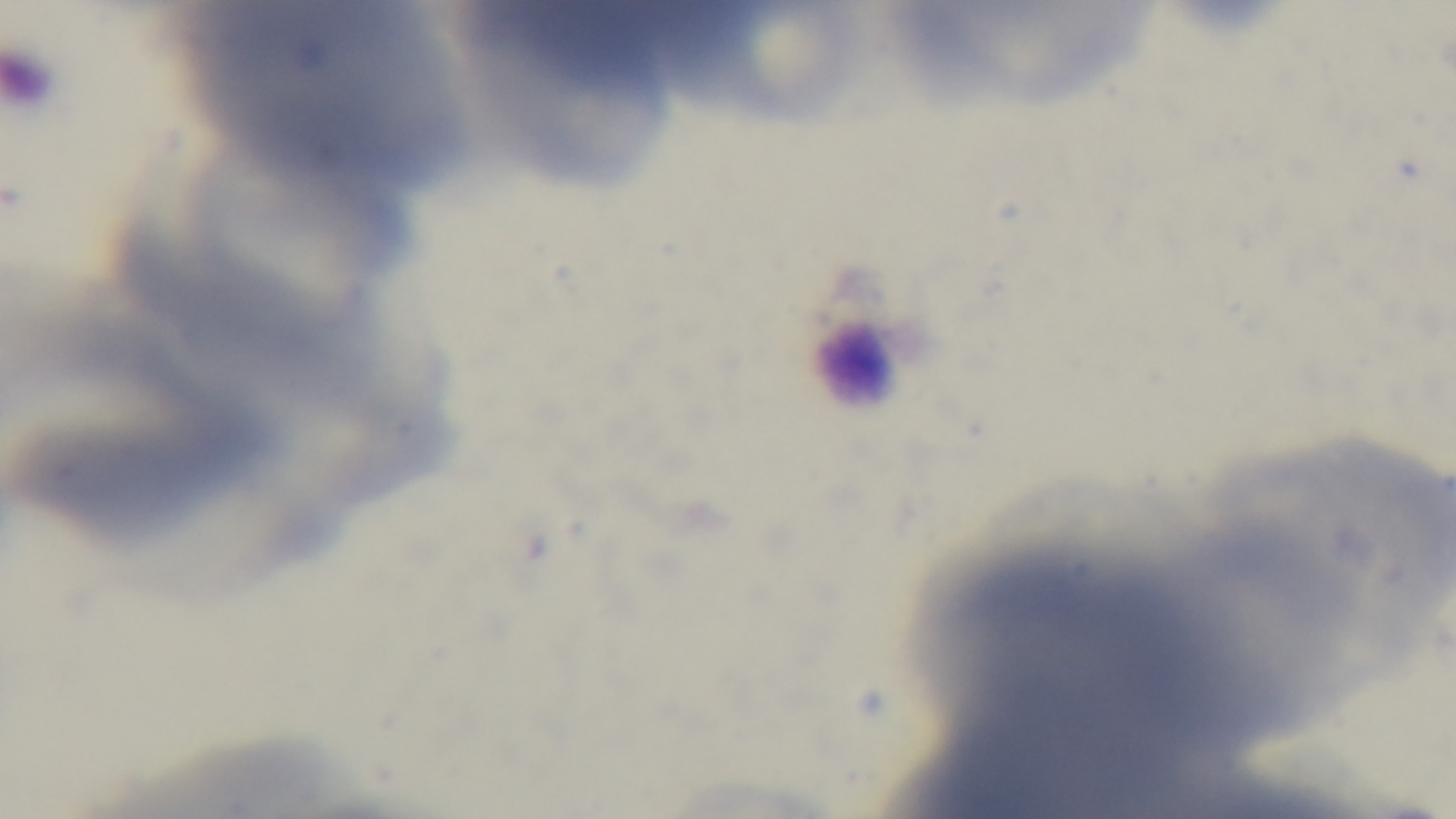

stain = Giemsa
capture = mounted 4K digital camera
preparation = thin blood film
malaria status = uninfected
modality = light microscopy
objective = 100x oil immersion
field of view = single